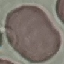

Malaria status: uninfected. Giemsa stain. Cell patch, automatically extracted from a larger field of view and resized to 64 × 64 pixels. Photographed with a smartphone camera at the microscope eyepiece. Thin blood smear.